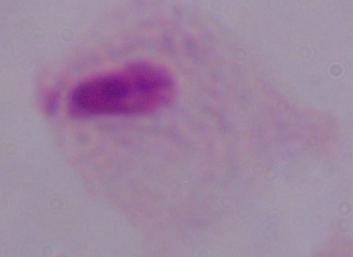

Summary:
  - Magnification: 1000x
  - Modality: micrograph
  - Identification: trichomonad